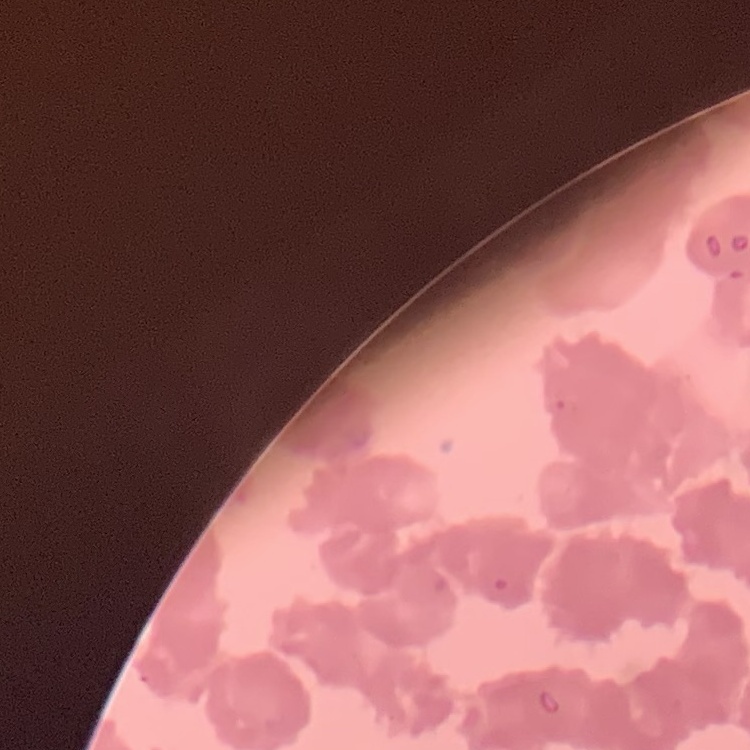

The erythrocytes exhibit rouleaux formation. One tile cut from a larger photomicrograph. Thin peripheral smear. Field's or Giemsa stain.